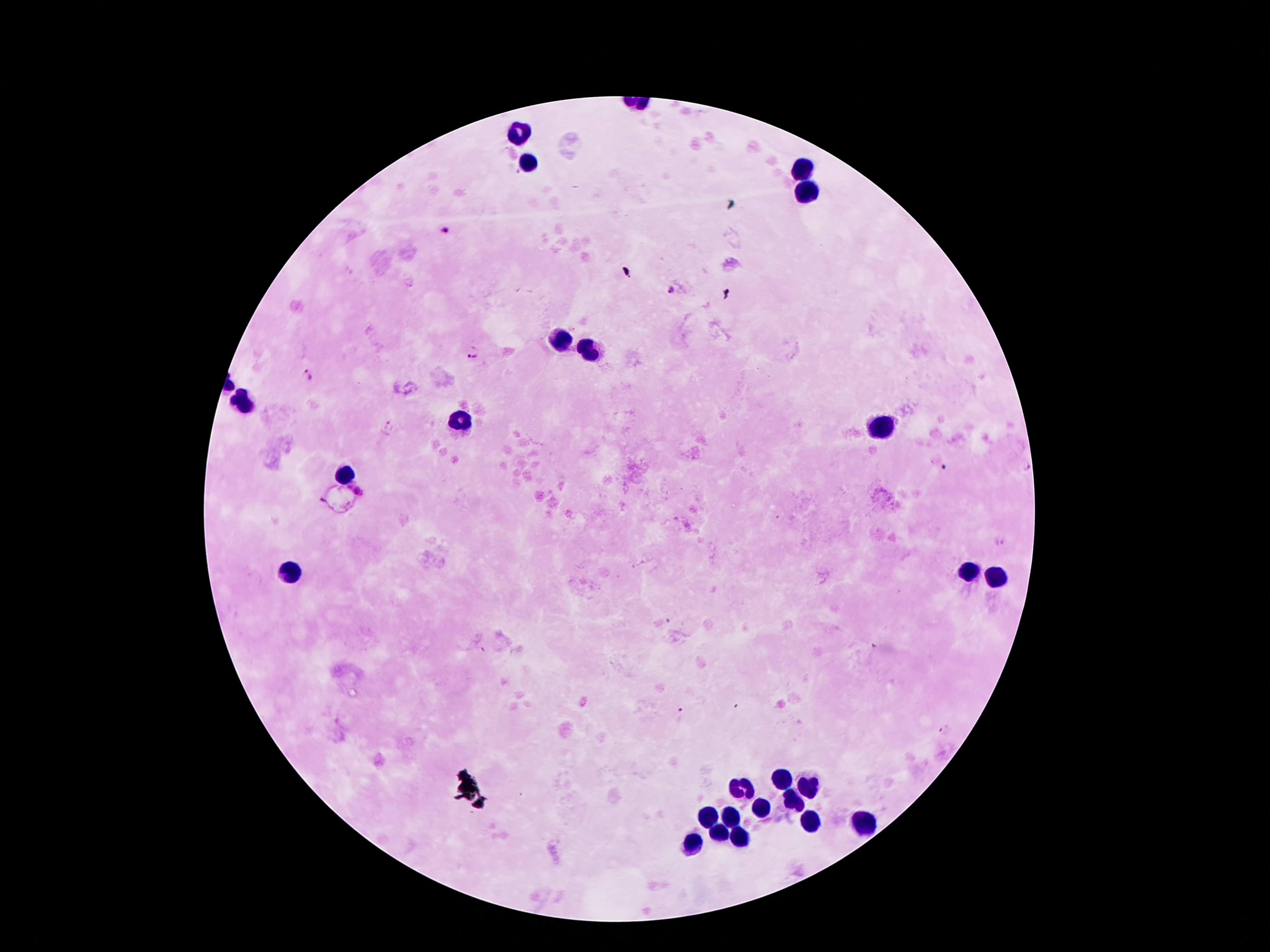

Approximate centers as (x, y) in pixels.
Summary:
  - Malaria parasite locations: (446, 229), (671, 290), (474, 354), (308, 376), (388, 425), (998, 543), (680, 713), (944, 729)
  - Leukocyte locations: (518, 134), (526, 161), (802, 170), (800, 191), (561, 338), (590, 348), (244, 406), (460, 420), (884, 428), (346, 475), (966, 571), (291, 574), (998, 579), (783, 779), (807, 786), (743, 788), (788, 801), (765, 808), (731, 816), (711, 818), (808, 820), (865, 821), (721, 831), (739, 833), (692, 845)
  - Patient malaria status: infected with Plasmodium falciparum
  - Capture: smartphone through the microscope eyepiece
  - Preparation: thick blood smear
  - Stain: Giemsa
  - Magnification: 100x
  - Image size: 1270×952 pixels
  - Field of view: one from this slide